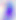

Photomicrograph. Toxoplasma gondii is shown. Captured at 400x magnification.